Evaluate for Plasmodium parasites.
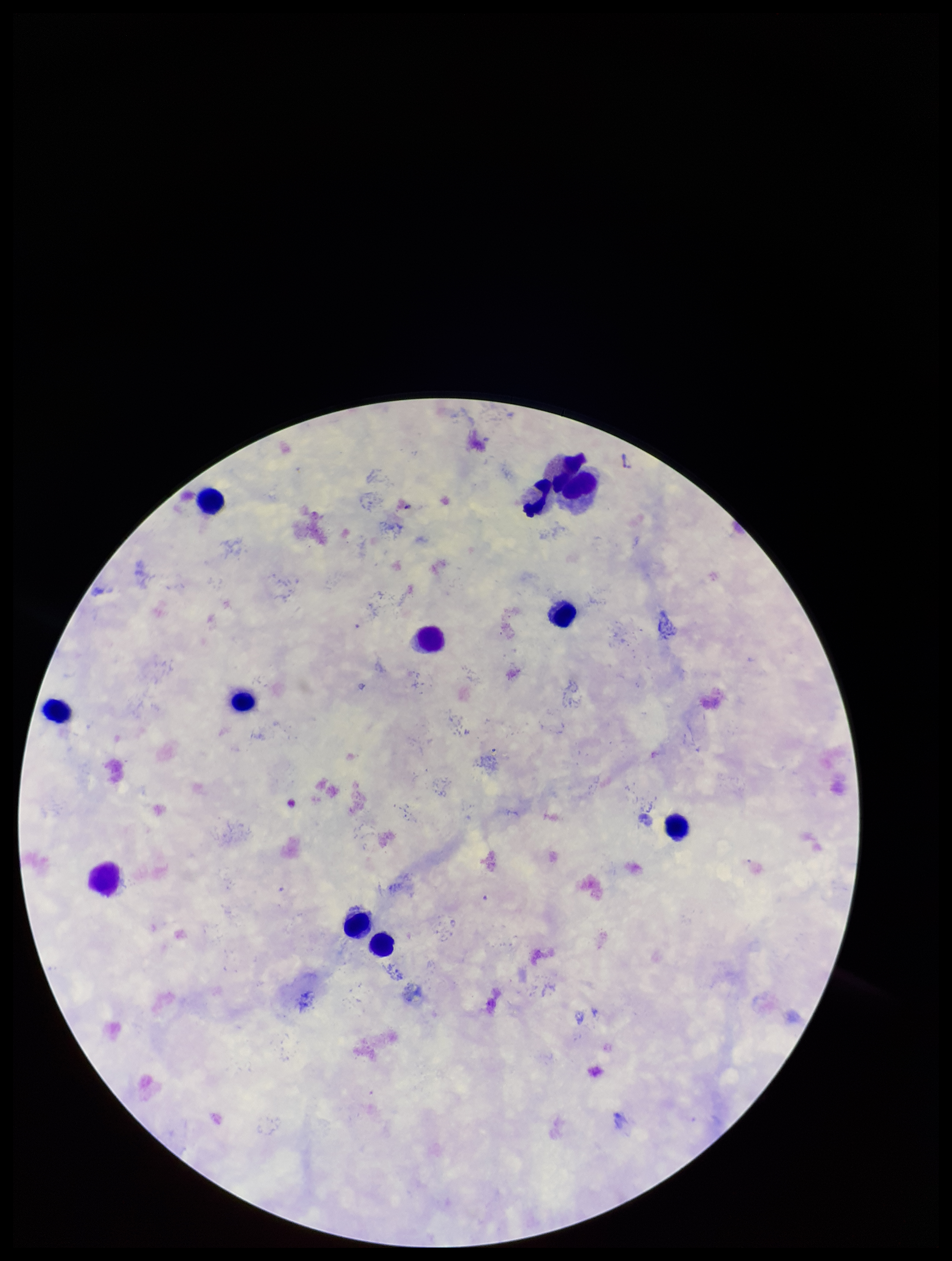
None identified.

species reported for this patient = Plasmodium falciparum
stain = Giemsa
preparation = thick
parasite count = 0
field of view = single
image size = 952×1261 pixels
leukocyte count = 11
patient malaria status = infected
capture = smartphone photograph through the microscope eyepiece